Give the extent of all Plasmodium ovale-infected red blood cells.
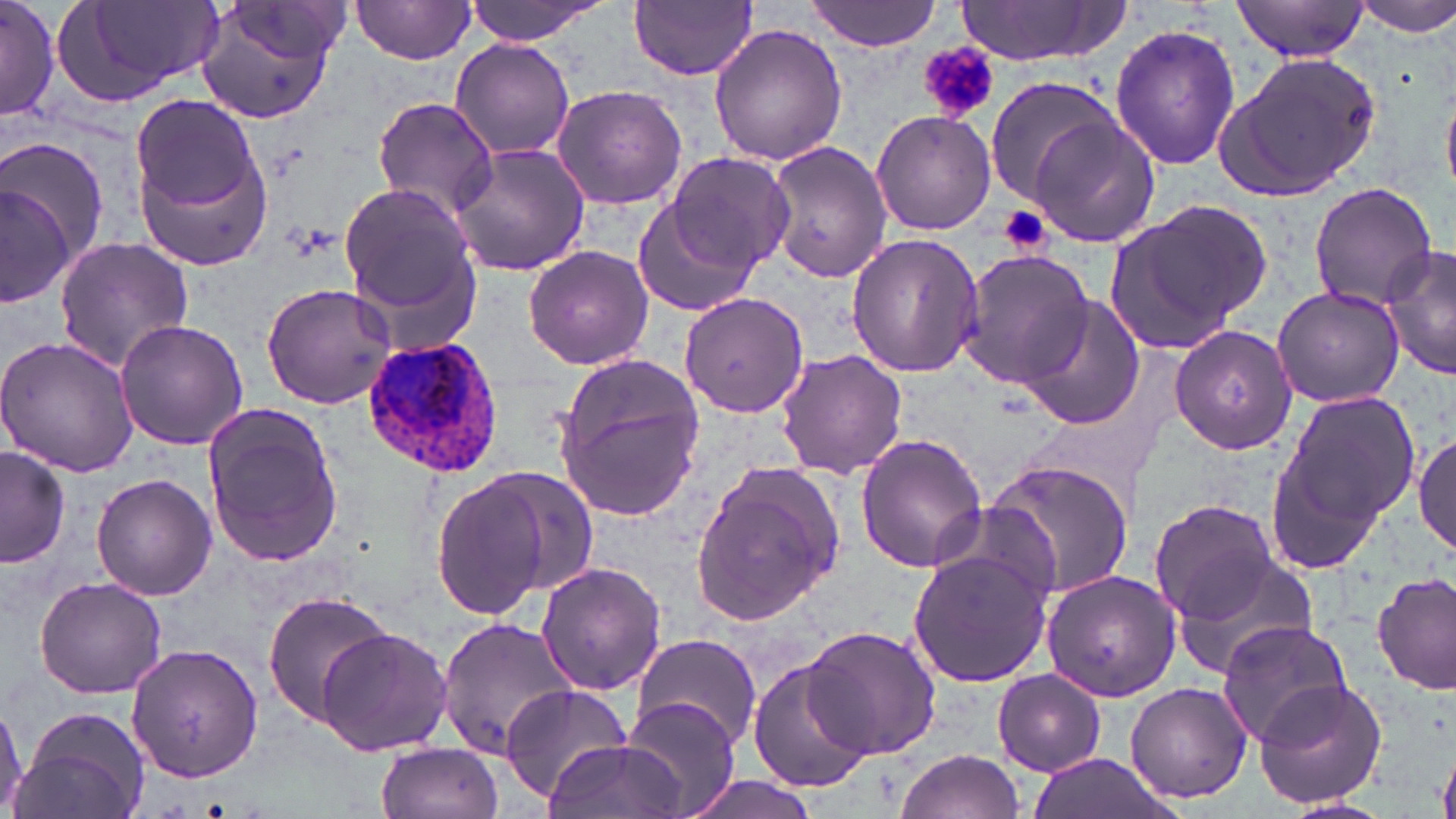
Approximate bounding boxes as (x1, y1, x2, y2) in pixels.
Plasmodium ovale-infected red blood cells: (361, 336, 506, 478).

Platelet locations: (918, 42, 1001, 122), (997, 206, 1052, 256). Uninfected red blood cell locations: (56, 0, 226, 108), (350, 0, 477, 63), (465, 0, 605, 45), (631, 0, 758, 81), (804, 0, 946, 51), (1233, 0, 1371, 62), (1353, 0, 1456, 35), (0, 1, 57, 120), (954, 1, 1131, 66), (196, 4, 343, 123), (708, 22, 846, 165), (1109, 24, 1242, 171), (450, 39, 576, 161), (1216, 53, 1381, 204), (983, 76, 1121, 208), (550, 84, 688, 210), (368, 96, 501, 221), (131, 98, 264, 218), (870, 109, 996, 236), (1028, 115, 1160, 248), (0, 137, 111, 263), (765, 140, 890, 283), (446, 143, 589, 278), (136, 150, 276, 271), (667, 152, 794, 272), (2, 177, 80, 311), (338, 179, 481, 322), (1309, 182, 1437, 310), (1104, 197, 1273, 353), (630, 200, 756, 318), (846, 233, 985, 378), (53, 235, 194, 373), (524, 245, 655, 370), (1380, 246, 1456, 381), (958, 250, 1095, 388), (261, 282, 397, 409), (1272, 286, 1404, 408), (681, 292, 809, 418), (1019, 294, 1144, 430), (114, 318, 247, 450), (1169, 324, 1297, 455), (0, 335, 139, 475), (776, 350, 908, 479), (552, 358, 704, 521), (1266, 386, 1422, 568), (202, 402, 343, 571), (1413, 430, 1456, 557), (855, 432, 988, 574), (0, 447, 70, 569), (980, 458, 1135, 600), (688, 461, 845, 630), (476, 468, 602, 597), (91, 474, 218, 601), (428, 476, 555, 621), (1149, 499, 1279, 623), (925, 505, 1062, 607), (908, 548, 1053, 686), (1170, 551, 1320, 683), (537, 562, 665, 695), (1040, 569, 1181, 702), (1374, 571, 1455, 696), (34, 576, 167, 699), (259, 592, 394, 723), (436, 618, 577, 763), (1216, 621, 1354, 746), (801, 624, 941, 759), (314, 627, 453, 756), (631, 633, 762, 751), (125, 642, 263, 783), (751, 661, 873, 794), (993, 669, 1105, 776), (1252, 675, 1387, 810), (1125, 680, 1253, 804), (500, 684, 634, 804), (625, 698, 739, 819), (0, 702, 27, 814), (11, 706, 152, 819), (545, 739, 685, 819), (375, 742, 503, 819), (894, 750, 1024, 819), (1028, 753, 1177, 819), (684, 775, 817, 819), (1282, 799, 1394, 819). Slide-level diagnosis: Plasmodium ovale. Light microscopy. Single field of view. Image is 1456×819 pixels. May-Grünwald-Giemsa-stained preparation. Thin blood smear. Captured at 1000x magnification.